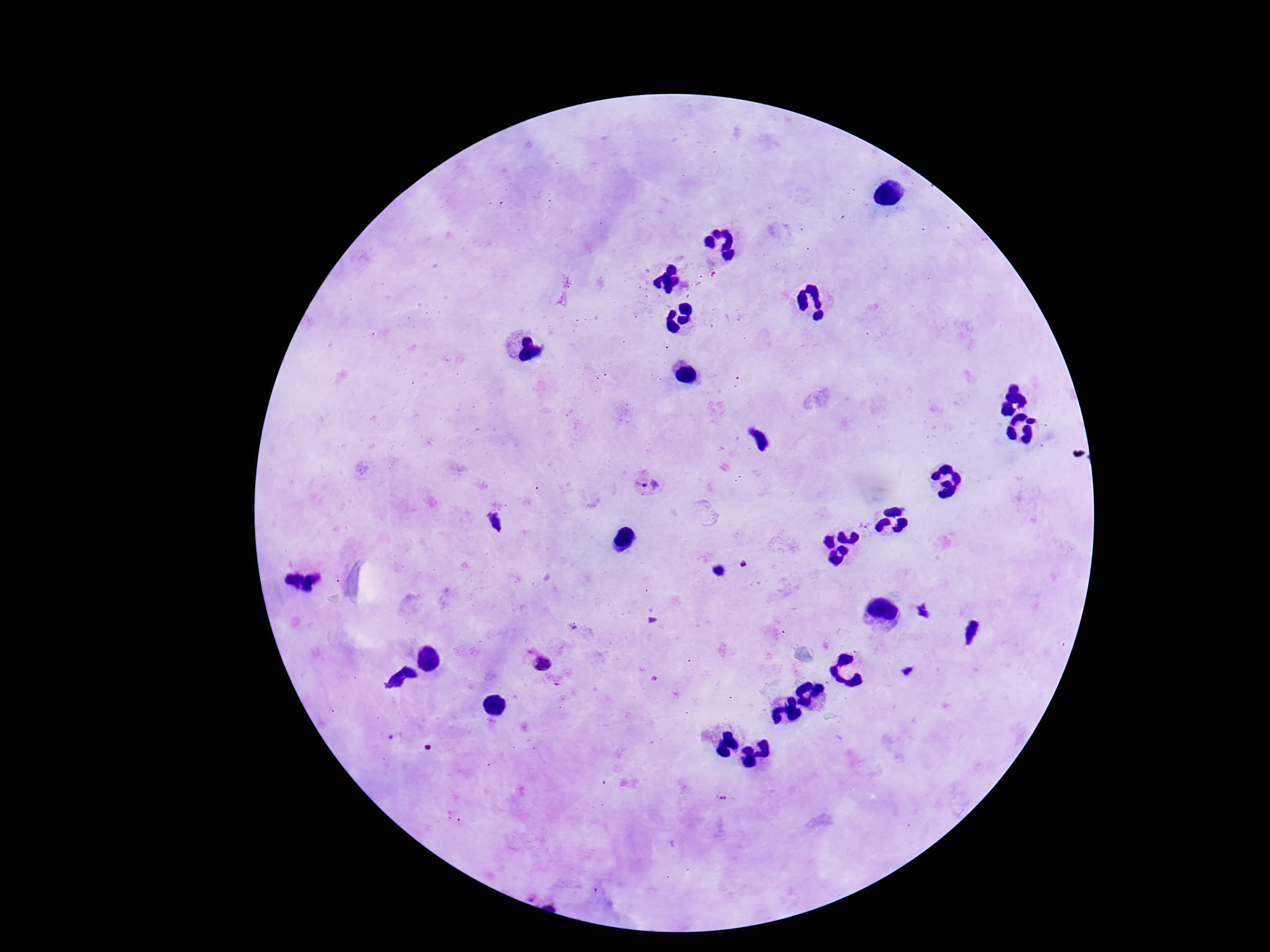

Approximate object centers, in pixels from the top-left corner. Plasmodium parasite locations: (x=649, y=486), (x=495, y=521), (x=540, y=659), (x=724, y=799). Image is 1270×952 pixels. Thick blood film. Patient malaria status: infected. 100x magnification. Giemsa stain. One field from this slide. Smartphone photograph taken through the microscope eyepiece.